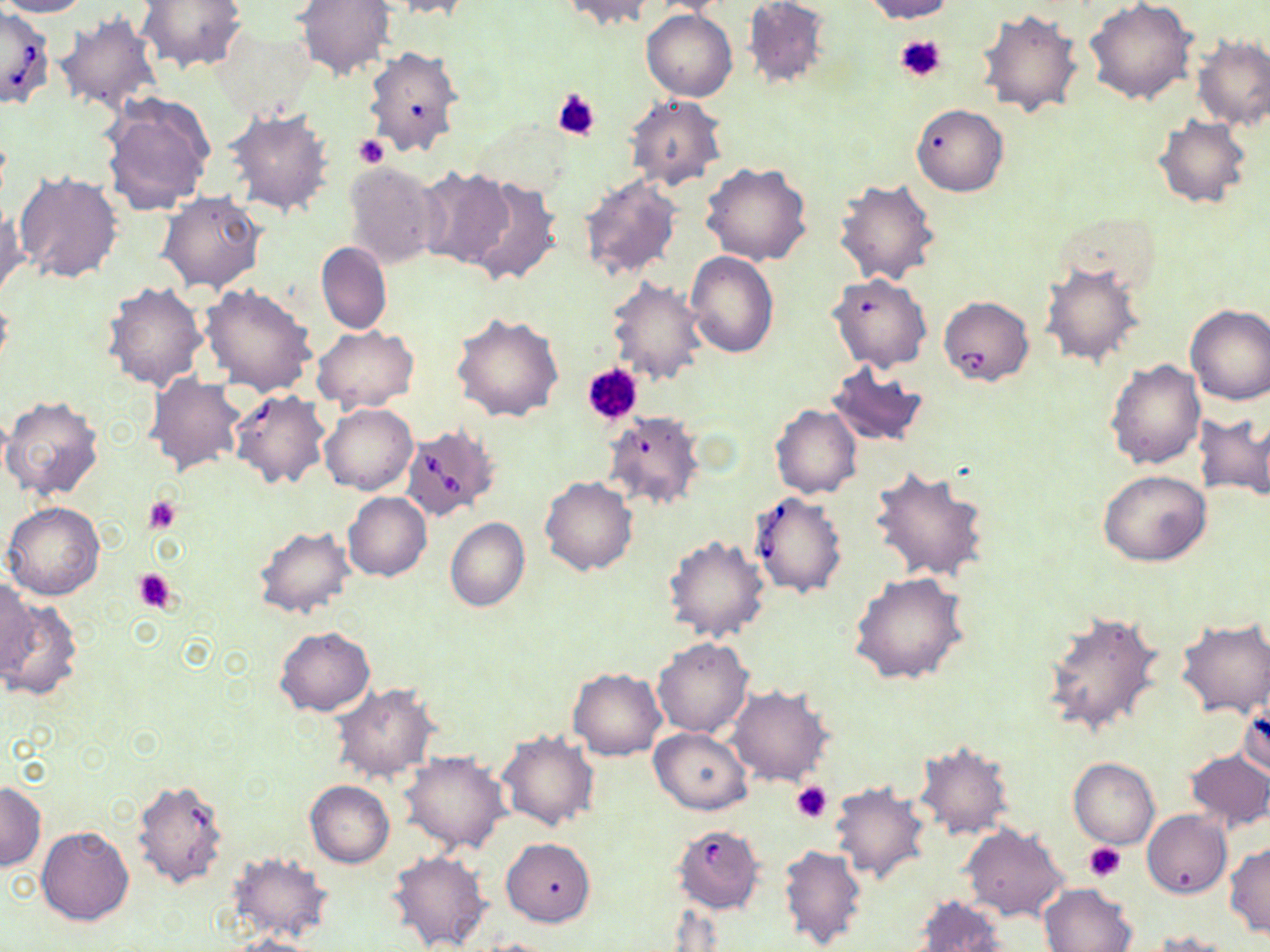

Approximate bounding boxes as (x1,y1)-(x2,y2) corner pairs in pixels. Platelet locations: (895,33)-(947,85), (551,87)-(601,142), (353,136)-(388,168), (583,362)-(644,425), (145,496)-(182,535), (133,567)-(176,614), (791,782)-(832,824), (1084,841)-(1126,881). Uninfected red blood cell locations: (0,0)-(91,18), (137,0)-(247,73), (383,0)-(473,19), (649,0)-(736,17), (743,0)-(830,90), (861,0)-(955,22), (1085,0)-(1197,104), (295,1)-(394,80), (555,1)-(656,30), (976,8)-(1085,118), (641,9)-(737,102), (54,13)-(163,113), (212,25)-(315,119), (1190,37)-(1270,131), (365,46)-(463,158), (99,93)-(213,216), (624,94)-(728,191), (911,103)-(1008,196), (226,109)-(334,217), (1153,116)-(1252,210), (343,161)-(444,267), (701,163)-(813,267), (415,166)-(512,267), (14,171)-(124,285), (577,174)-(683,282), (462,177)-(562,286), (833,177)-(939,287), (158,191)-(267,293), (0,203)-(27,302), (1056,211)-(1162,297), (317,242)-(392,336), (686,250)-(779,358), (1040,262)-(1144,368), (829,272)-(933,373), (606,275)-(708,384), (102,282)-(207,392), (201,284)-(317,395), (1184,303)-(1270,404), (451,313)-(565,422), (311,324)-(417,414), (1104,359)-(1206,469), (826,362)-(931,449), (146,373)-(246,478), (229,390)-(330,489), (1,396)-(104,502), (320,402)-(418,496), (769,403)-(862,498), (1193,412)-(1270,505), (868,465)-(990,582), (1098,469)-(1211,566), (539,475)-(638,576), (343,492)-(432,581), (3,501)-(106,600), (445,517)-(529,612), (252,525)-(356,619), (662,534)-(770,644), (850,572)-(970,686), (0,577)-(36,681), (0,595)-(83,703), (1040,610)-(1166,737), (1176,618)-(1270,718), (275,627)-(375,715), (653,637)-(752,737), (568,667)-(666,760), (331,684)-(439,783), (726,685)-(833,786), (1238,694)-(1269,780), (355,695)-(495,817), (650,727)-(753,814), (497,731)-(598,832), (913,743)-(1014,840), (1183,750)-(1270,832), (400,752)-(509,854), (1069,757)-(1159,849), (131,779)-(230,890), (305,780)-(394,866), (830,780)-(930,884), (0,782)-(46,871), (1142,810)-(1231,898), (961,824)-(1069,922), (37,826)-(134,926), (502,837)-(595,927), (778,842)-(866,950), (1225,843)-(1270,939), (385,848)-(492,952), (226,851)-(334,945), (1039,883)-(1137,952), (912,894)-(1009,952), (1151,931)-(1239,952), (227,934)-(325,952), (472,937)-(565,951). Babesia divergens-infected red blood cell locations: (0,5)-(54,108), (940,295)-(1031,387), (604,410)-(705,511), (398,424)-(500,522), (750,491)-(849,599), (673,826)-(770,916). Slide-level diagnosis: Babesia divergens. May-Grünwald-Giemsa stain. Thin blood smear. 1000x magnification. Single field of view. Light microscopy. Image is 1270×952 pixels.